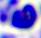
Summary:
  - Modality: micrograph
  - Magnification: 400x
  - Identification: white blood cell